State which parasite is depicted.
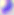
This is Toxoplasma gondii.

Summary:
  - Modality: micrograph
  - Magnification: 400x